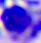 A white blood cell is shown. Captured at 400x magnification. Photomicrograph.